Point out each Plasmodium parasite.
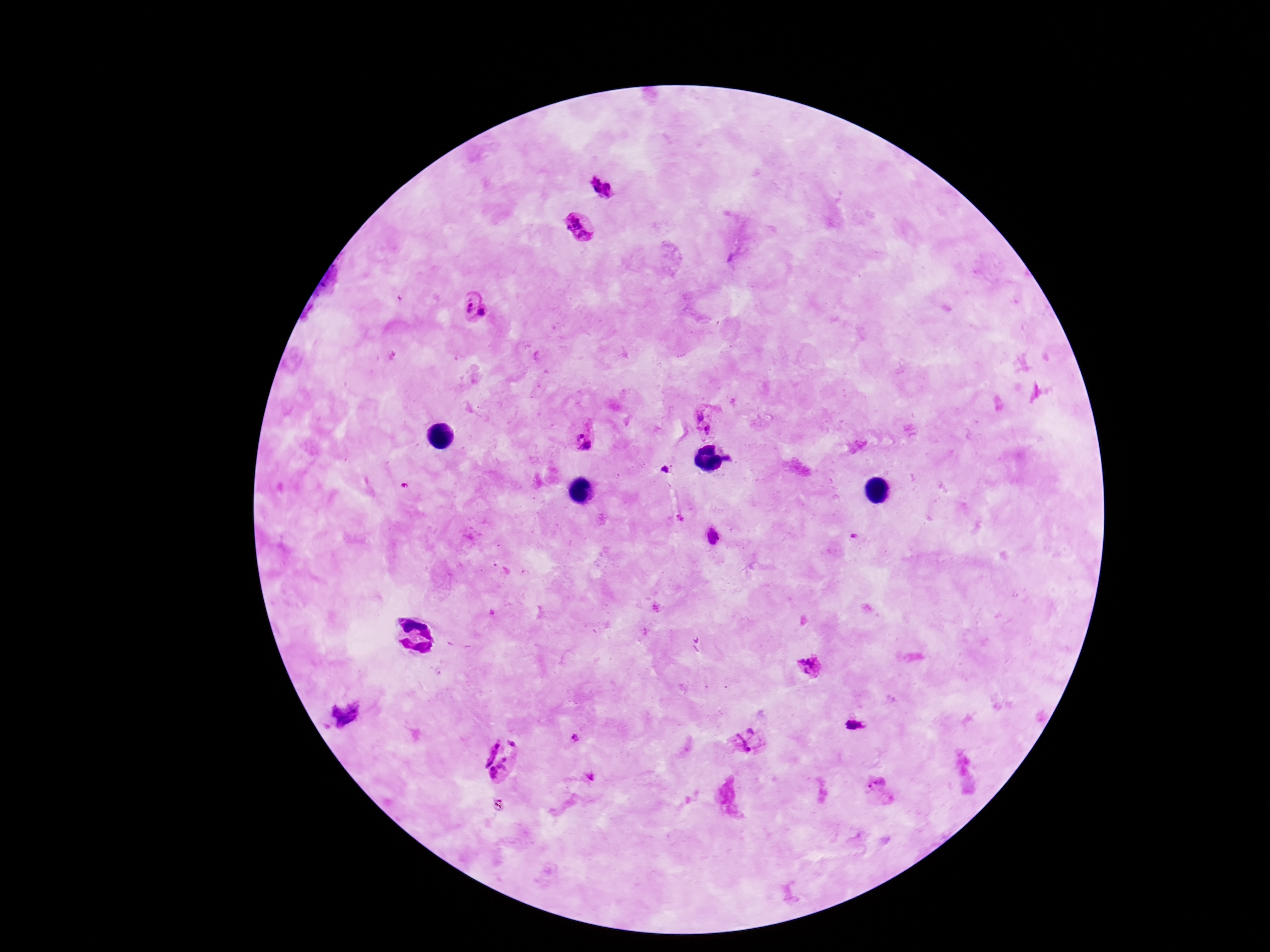
Approximate centers as {x, y} in pixels.
Plasmodium parasites: {601, 189}, {579, 228}, {476, 306}, {708, 421}, {581, 435}, {810, 667}, {854, 725}, {575, 737}, {749, 740}, {499, 759}, {878, 791}.

Summary:
  - Patient malaria status: positive
  - Field of view: single
  - Stain: Giemsa
  - Magnification: 100x
  - Preparation: thick blood film
  - Capture: smartphone camera through the microscope eyepiece
  - Image size: 1270×952 pixels